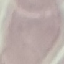
malaria status = uninfected
stain = Giemsa
image type = automatically extracted cell patch, resized to 64 × 64 pixels
capture = smartphone through the microscope eyepiece
preparation = thin smear